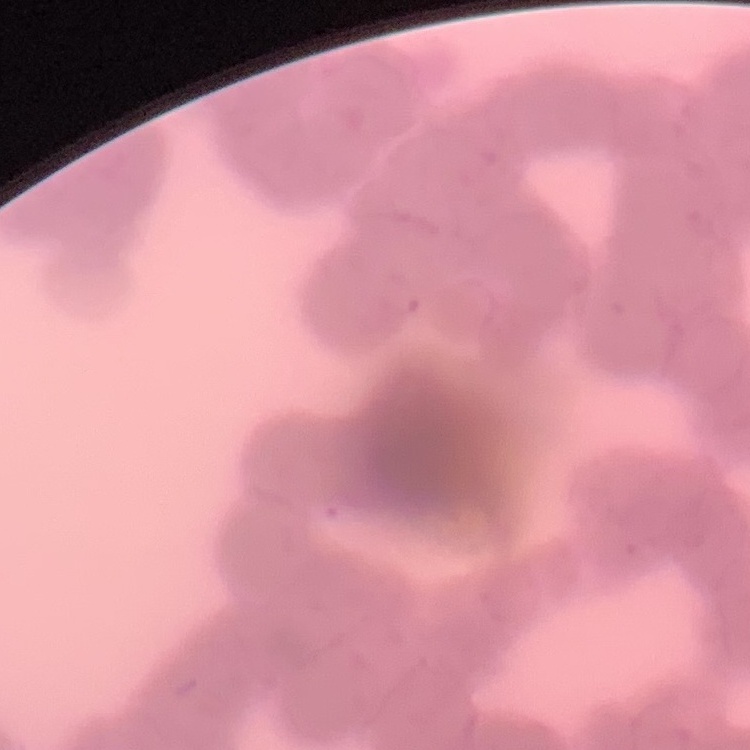

The erythrocytes show rouleaux formation. Thin blood film. Field's or Giemsa stain. One tile cut from a larger photomicrograph.